State the preparation type.
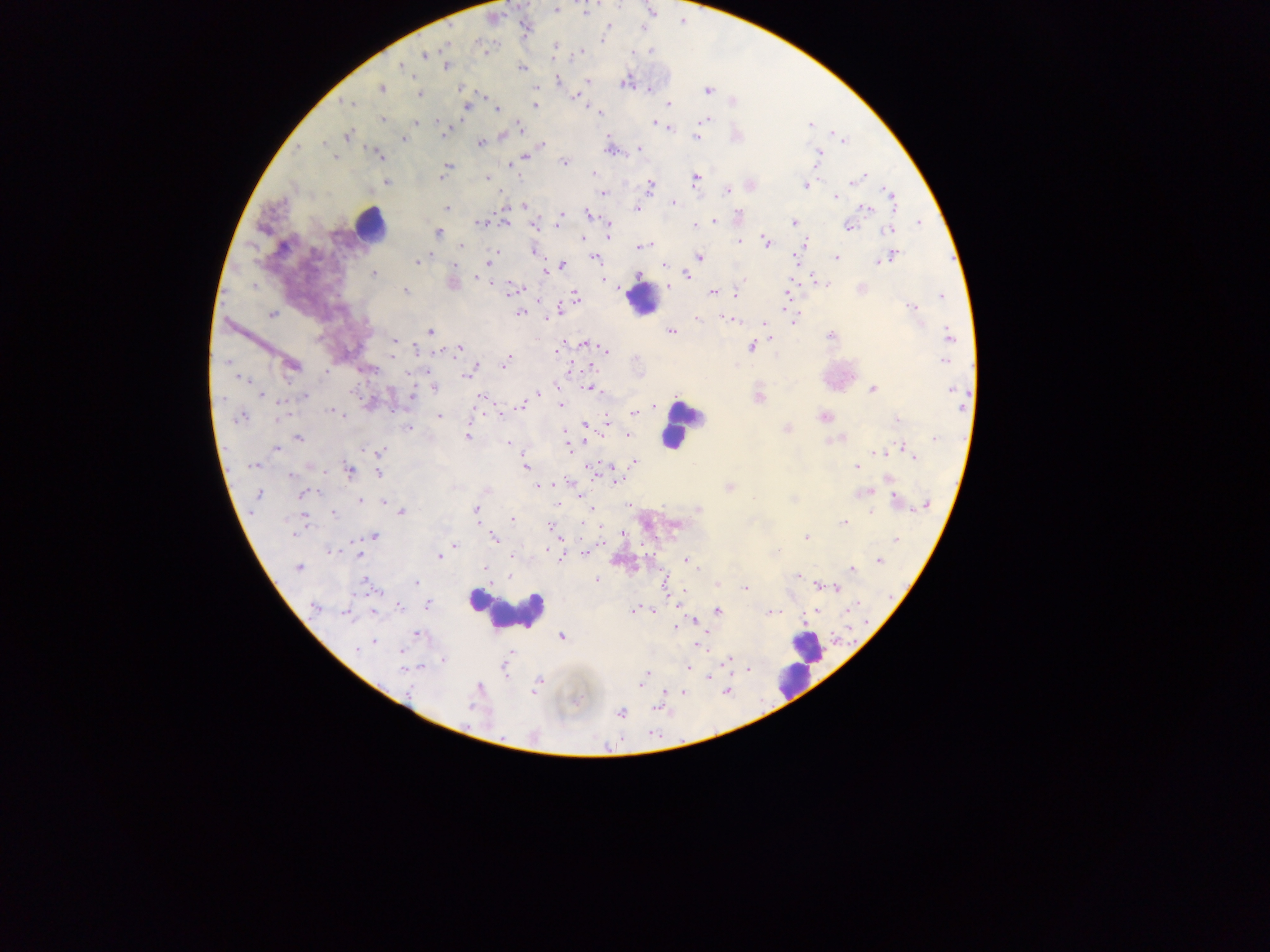
Thick blood smear.

field_of_view: single
malaria_parasite_locations: 'approximate centers as (x, y) in pixels: (556, 8), (607, 27), (603, 39), (482, 46), (555, 46), (650, 51), (633, 52), (580, 53), (424, 54), (401, 66), (447, 66), (522, 67), (559, 80), (586, 81), (626, 82), (381, 87), (460, 89), (709, 90), (419, 95), (578, 96), (346, 103), (669, 103), (534, 104), (466, 106), (497, 109), (598, 111), (382, 120), (705, 120), (417, 121), (655, 124), (810, 125), (661, 127), (521, 128), (669, 129), (444, 132), (347, 135), (503, 135), (696, 138), (404, 140), (845, 141), (324, 143), (479, 143), (542, 144), (298, 148), (639, 148), (609, 150), (818, 154), (378, 155), (525, 158), (334, 159), (564, 162), (511, 164), (447, 167), (443, 173), (594, 173), (486, 177), (862, 177), (696, 179), (857, 180), (386, 182), (805, 185), (650, 186), (727, 191), (602, 194), (835, 197), (891, 197), (673, 203), (524, 205), (446, 208), (867, 208), (637, 209), (588, 214), (738, 215), (561, 218), (713, 221), (480, 222), (506, 222), (794, 223), (534, 224), (848, 225), (610, 226), (694, 226), (889, 230), (438, 232), (609, 234), (583, 238), (740, 241), (766, 241), (805, 244), (646, 245), (461, 246), (640, 247), (535, 252), (894, 255), (699, 256), (428, 257), (595, 258), (837, 258), (417, 261), (489, 262), (879, 262), (663, 264), (562, 265), (545, 271), (691, 271), (373, 274), (687, 275), (745, 279), (482, 280), (453, 283), (821, 283), (668, 286), (514, 289), (405, 291), (713, 292), (736, 294), (576, 296), (942, 296), (912, 307), (558, 311), (521, 313), (272, 315), (698, 319), (729, 319), (793, 321), (764, 323), (429, 331), (670, 332), (831, 335), (949, 336), (395, 342), (586, 344), (752, 347), (458, 349), (559, 349), (417, 350), (605, 350), (944, 361), (505, 363), (292, 366), (469, 373), (243, 380), (434, 388), (590, 388), (873, 390), (954, 391), (261, 394), (537, 394), (305, 396), (413, 396), (482, 397), (759, 398), (521, 405), (562, 405), (654, 406), (335, 412), (634, 413), (439, 416), (239, 417), (824, 417), (897, 420), (607, 423), (586, 427), (407, 428), (787, 429), (628, 433), (467, 436), (299, 438), (838, 438), (935, 439), (508, 444), (569, 448), (276, 449), (876, 451), (908, 451), (380, 452), (913, 454), (634, 461), (253, 466), (526, 466), (856, 467), (349, 470), (379, 473), (289, 476), (616, 480), (539, 486), (730, 488), (866, 492), (258, 494), (303, 494), (360, 500), (897, 500), (385, 503), (927, 504), (698, 509), (401, 511), (477, 511), (871, 513), (334, 514), (304, 518), (513, 518), (844, 523), (551, 526), (554, 530), (374, 537), (806, 537), (493, 538), (896, 540), (455, 545), (330, 551), (777, 551), (585, 553), (359, 554), (513, 556), (439, 557), (687, 560), (879, 561), (298, 568), (852, 569), (485, 570), (798, 575), (597, 580), (367, 583), (416, 583), (665, 584), (718, 584), (820, 586), (745, 588), (837, 589), (314, 605), (428, 605), (399, 607), (718, 610), (634, 611), (651, 611), (773, 611), (374, 612), (346, 614), (416, 634), (561, 636), (374, 642), (699, 644), (358, 649), (400, 652), (728, 659), (443, 661), (689, 667), (404, 669), (505, 671), (646, 675), (642, 682), (537, 684), (727, 691), (683, 692), (621, 713)'
capture: mobile-phone photograph through a microscope
country: Ghana
image_size: 1270×952 pixels
leukocyte_locations: 'approximate centers as (x, y) in pixels: (369, 225), (644, 299), (677, 426), (505, 610), (806, 647), (801, 658)'